Give the position of each Plasmodium falciparum parasite with its life-cycle stage, each leukocyte, and any debris.
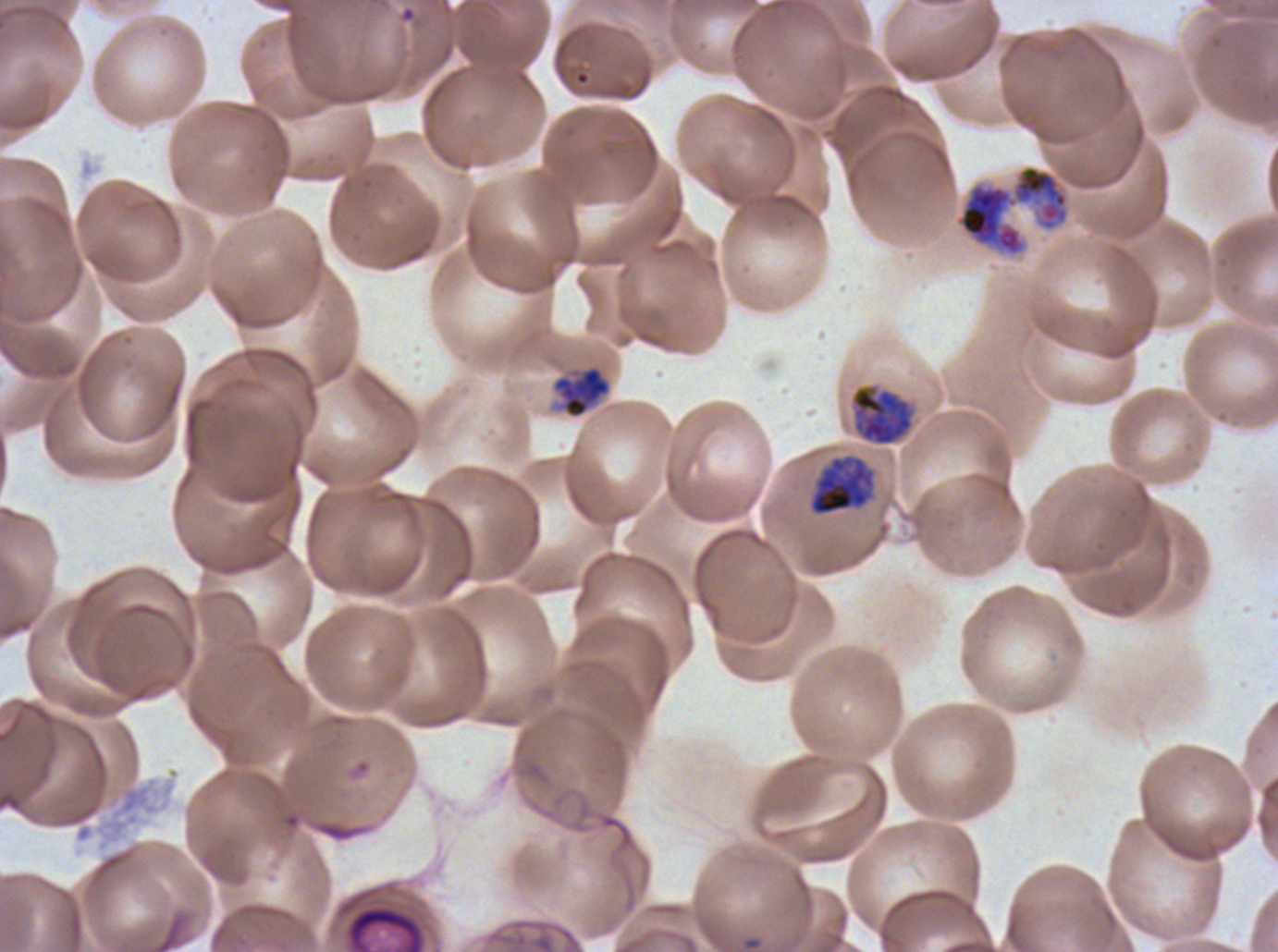
Approximate bounding boxes as [x1, y1, x2, y2] in pixels.
Mid trophozoites: [553, 366, 610, 419].
Late trophozoites: [958, 185, 1023, 254], [850, 384, 914, 446], [808, 455, 876, 516].
Debris: [343, 903, 428, 951].
No rings, late-ring/early-trophozoite forms, early schizonts, late schizonts, segmenters, gametocytes, or leukocytes observed.

A sub-image separated from a larger composite. Giemsa-stained preparation. Image is 1278×952 pixels. Life-cycle stages observed: mid trophozoite, late trophozoite. Thin blood film. Plasmodium falciparum cultured ex vivo for 24 to 48 hours, from a patient in The Gambia.